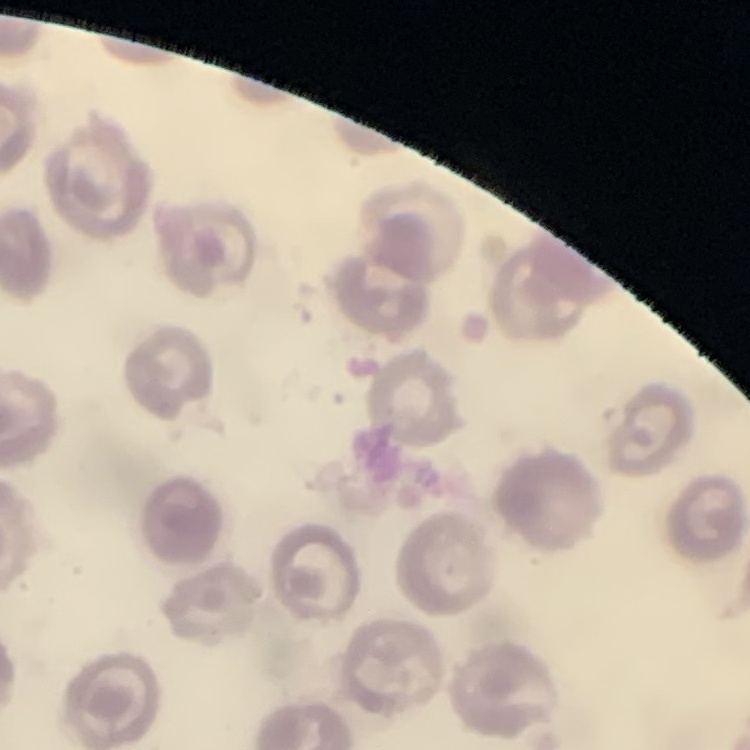
{
  "erythrocyte_morphology": "no rouleaux formation",
  "preparation": "thin blood film",
  "stain": "Field's or Giemsa",
  "image_type": "one tile cut from a larger photomicrograph"
}